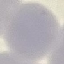
malaria status = uninfected
capture = smartphone through the microscope eyepiece
preparation = thin smear
stain = Giemsa
image type = automatically extracted cell patch, resized to 64 × 64 pixels